Comment on the morphology of the erythrocytes.
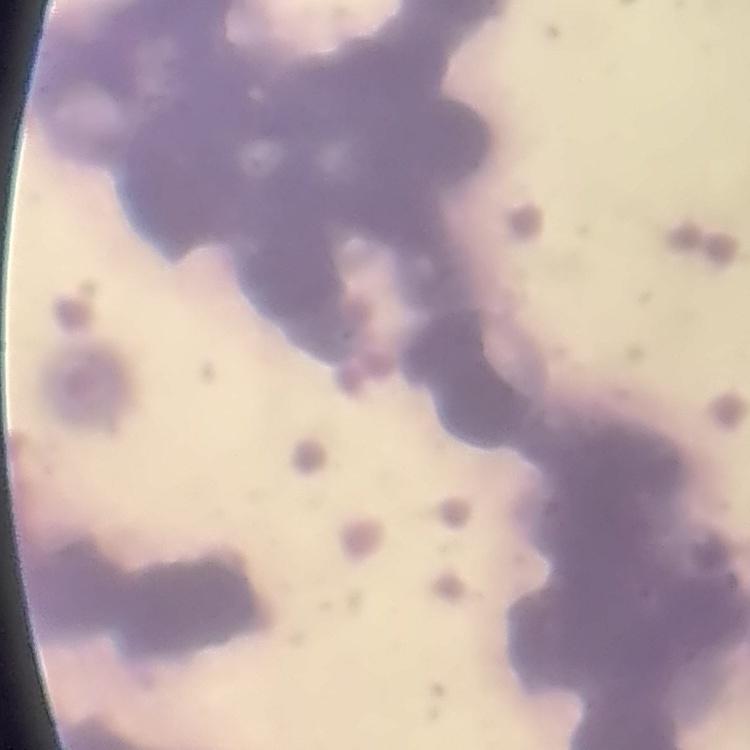

They show rouleaux formation.

Stained with either Field's or Giemsa. Thin blood film. Square crop of a larger photomicrograph.